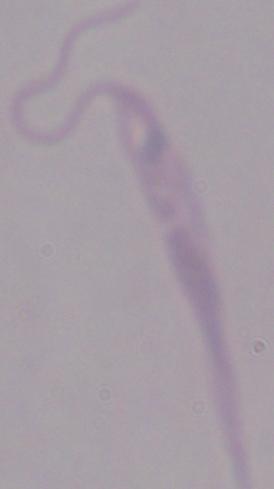
magnification = 1000x
modality = photomicrograph
identification = Leishmania